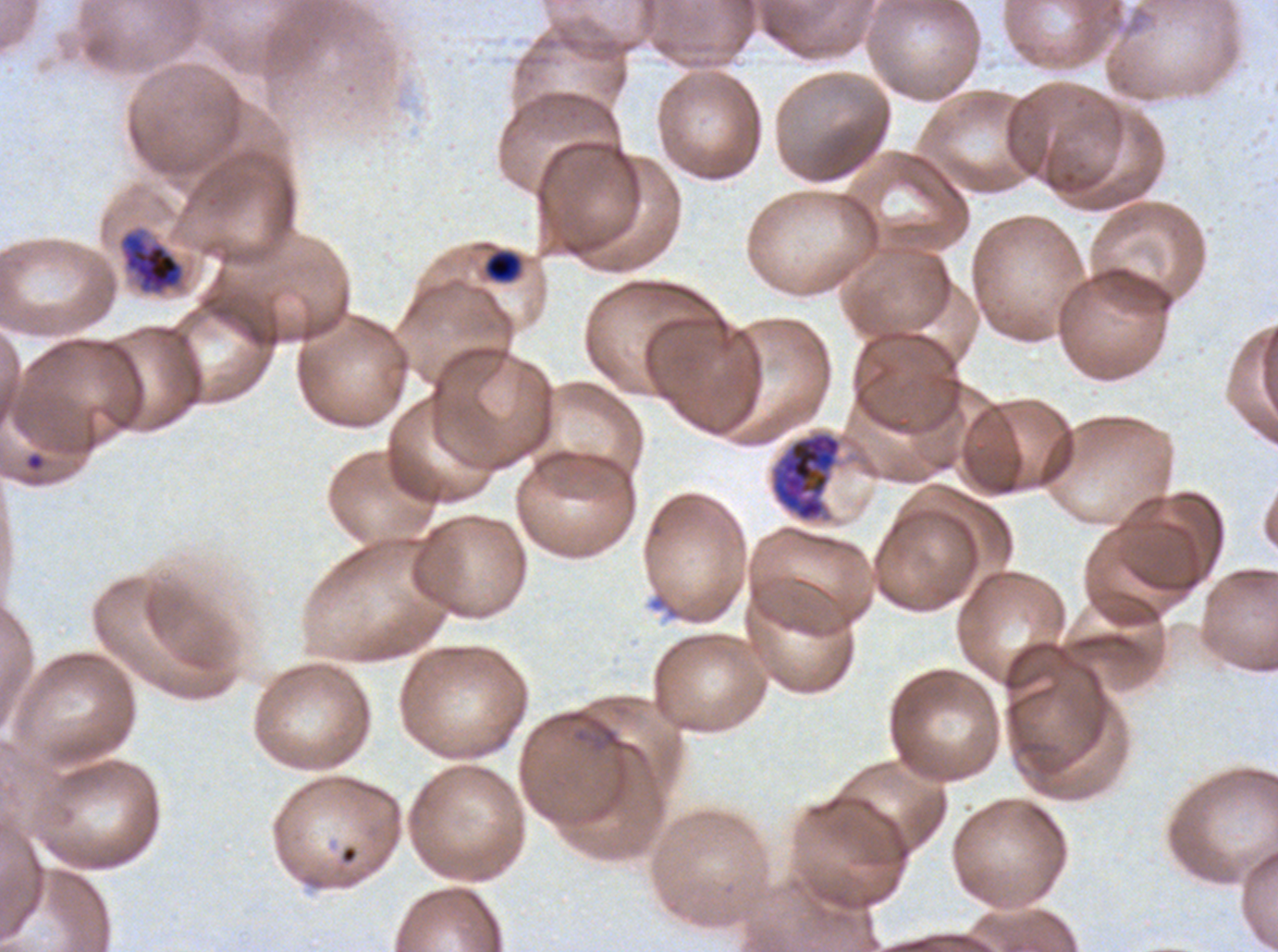

Approximate bounding boxes as [x1, y1, x2, y2] in pixels. Early schizont locations: [770, 431, 842, 521]. Ring locations: [26, 453, 44, 470]. Late-ring/early-trophozoite locations: [485, 251, 520, 281]. Late trophozoite locations: [122, 232, 183, 292]. Thin blood film. Life-cycle stages observed: ring, late-ring/early-trophozoite, late trophozoite, early schizont. One sub-image of a larger composite. Ex-vivo Plasmodium falciparum culture from a patient in The Gambia, grown for 24 to 48 hours. Image is 1278×952 pixels. Giemsa-stained preparation.